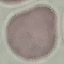
result: no malaria parasites seen
preparation: thin blood smear
capture: smartphone camera at the microscope eyepiece
image_type: automatically extracted cell patch, resized to 64 × 64 pixels
stain: Giemsa